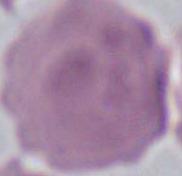
identification = red blood cell
magnification = 1000x
modality = photomicrograph